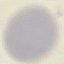
Result: negative for malaria parasites. Automatically extracted cell patch, resized to 64 × 64 pixels. Photographed with a smartphone camera at the microscope eyepiece. Giemsa stain. Thin smear of blood.